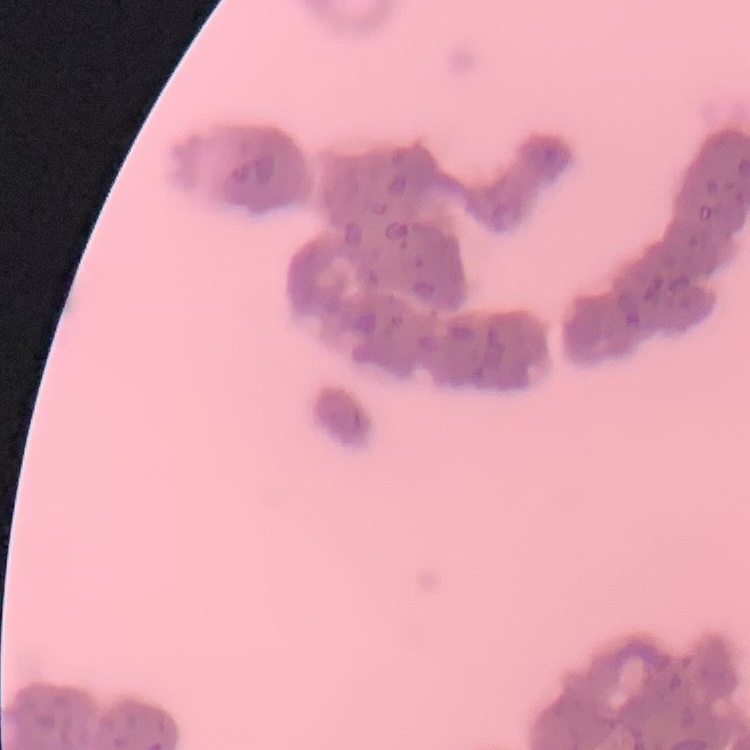

Summary:
  - Erythrocyte morphology: rouleaux formation
  - Stain: Field's or Giemsa
  - Image type: square crop of a larger photomicrograph
  - Preparation: thin blood film